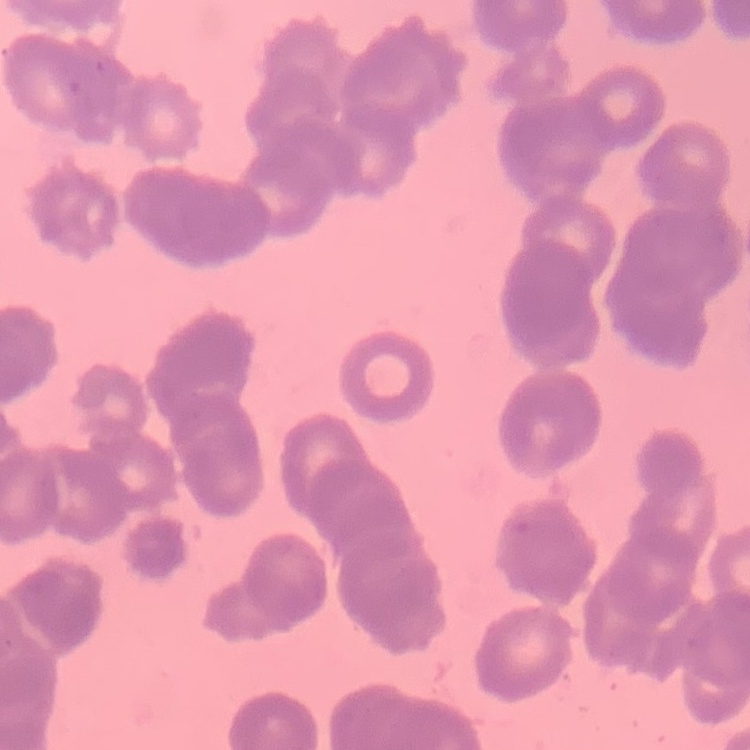

Summary:
  - Red blood cell morphology: rouleaux formation
  - Preparation: thin blood film
  - Image type: one tile cut from a larger photomicrograph
  - Stain: Field's or Giemsa